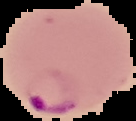

Summary:
  - Malaria status: parasitized
  - Preparation: thin blood film
  - Image size: 136×121 pixels
  - Image type: cell region segmented out of the field of view; surrounding area masked to black